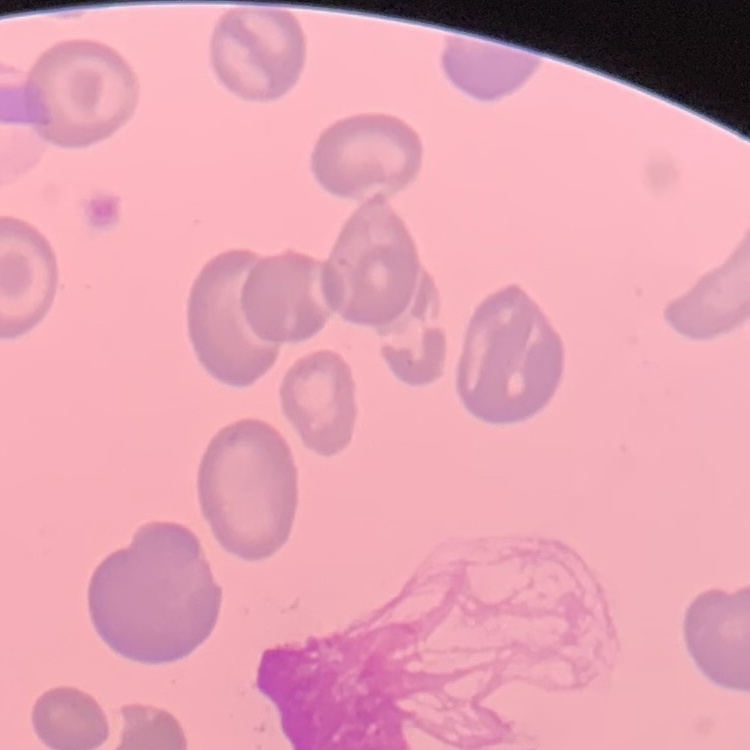
red blood cell morphology = no rouleaux formation
preparation = thin blood smear
image type = square crop of a larger photomicrograph
stain = Field's or Giemsa